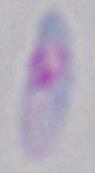

{
  "identification": "Toxoplasma gondii",
  "modality": "photomicrograph",
  "magnification": "1000x"
}